Describe the morphology of the erythrocytes.
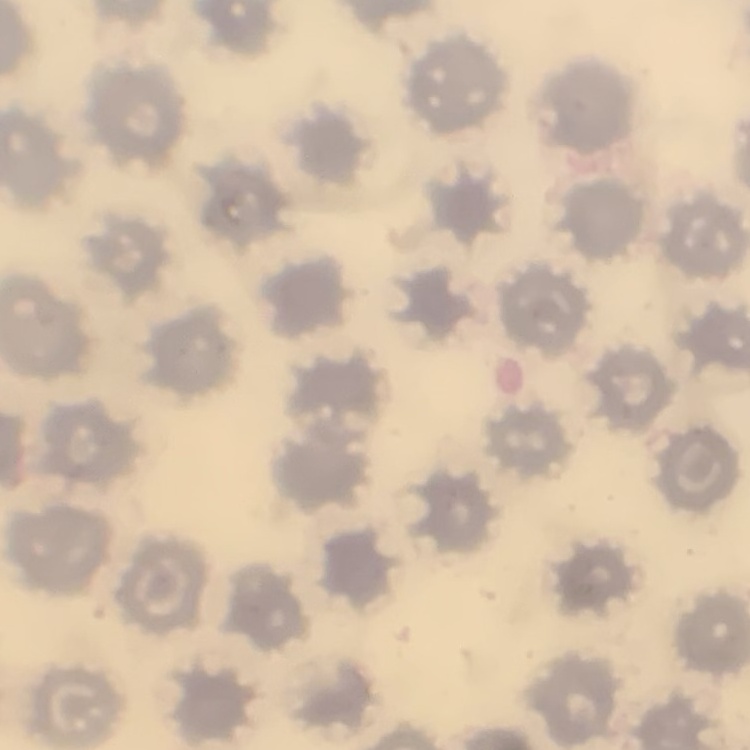
No rouleaux formation.

Stained with either Field's or Giemsa. Square crop of a larger photomicrograph. Thin blood smear.